Locate every Plasmodium parasite and every leukocyte.
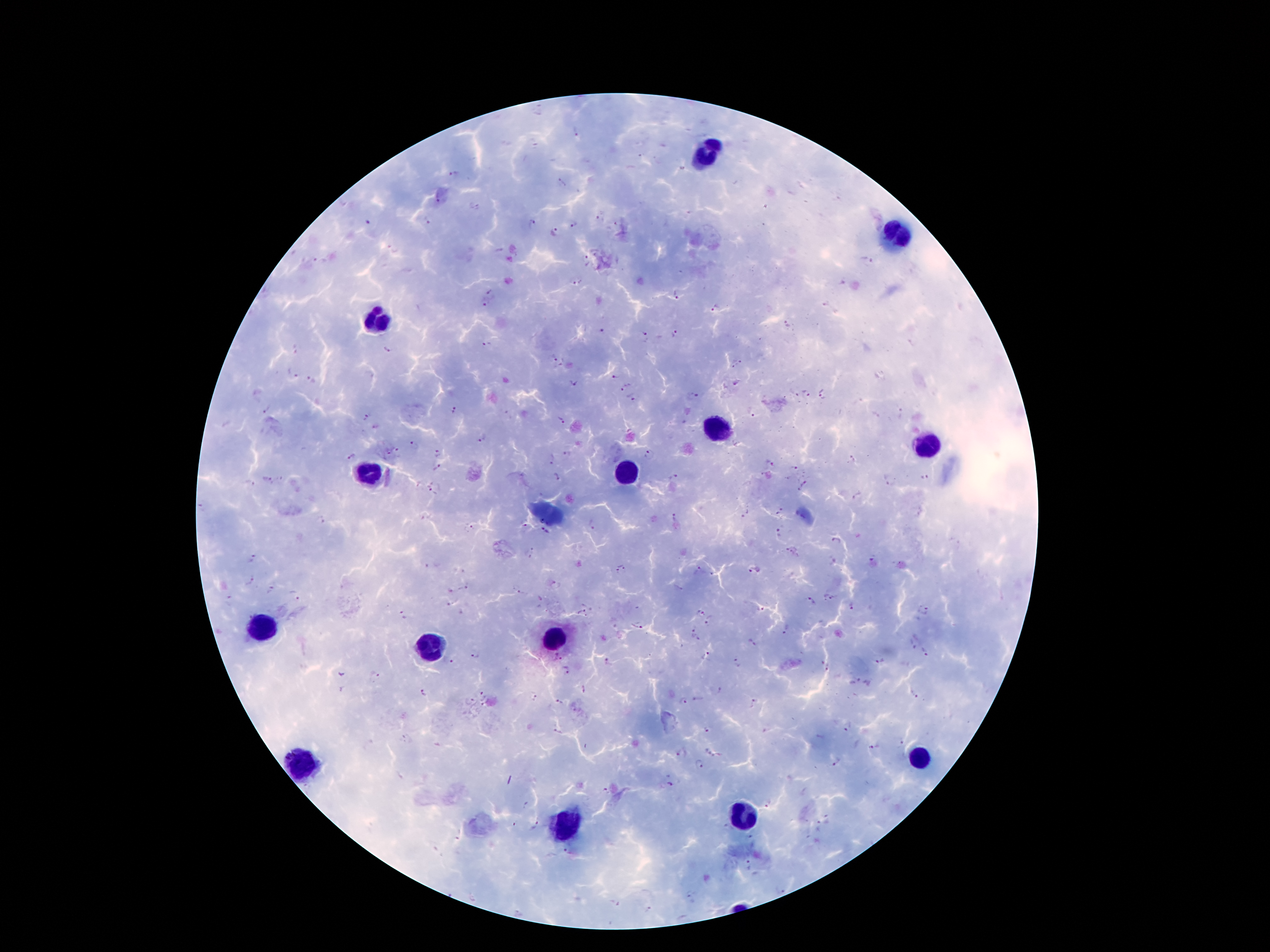

Approximate centers as (x, y) in pixels.
Plasmodium parasites: (538, 111), (577, 134), (452, 176), (560, 183), (437, 200), (473, 207), (427, 221), (531, 223), (572, 223), (553, 232), (391, 249), (586, 259), (316, 260), (867, 260), (577, 282), (492, 291), (676, 297), (486, 304), (716, 309), (788, 326), (601, 332), (676, 335), (647, 339), (487, 344), (297, 350), (386, 351), (552, 358), (736, 363), (291, 376), (613, 377), (312, 382), (573, 382), (625, 387), (806, 392), (792, 395), (823, 396), (631, 398), (692, 398), (267, 409), (456, 409), (748, 413), (901, 414), (874, 415), (366, 417), (559, 421), (483, 438), (414, 446), (399, 450), (386, 453), (440, 453), (566, 453), (650, 455), (350, 457), (851, 460), (552, 462), (768, 463), (438, 467), (795, 467), (925, 476), (557, 477), (673, 477), (886, 479), (268, 481), (247, 484), (804, 484), (433, 489), (858, 495), (781, 510), (744, 514), (426, 518), (673, 519), (321, 520), (539, 520), (590, 524), (525, 526), (469, 528), (544, 531), (778, 534), (836, 540), (790, 551), (531, 552), (251, 558), (870, 561), (430, 566), (622, 569), (698, 569), (754, 571), (250, 581), (555, 585), (466, 588), (270, 590), (520, 591), (295, 595), (827, 597), (230, 600), (810, 601), (447, 604), (851, 608), (761, 609), (923, 611), (700, 613), (581, 614), (403, 617), (709, 621), (637, 626), (786, 628), (692, 632), (752, 642), (912, 645), (926, 653), (474, 656), (706, 656), (556, 659), (449, 660), (880, 661), (607, 662), (738, 663), (824, 669), (342, 672), (567, 673), (376, 674), (585, 687), (343, 688), (721, 689), (423, 693), (483, 694), (914, 695), (535, 699), (697, 699), (468, 701), (559, 701), (684, 701), (754, 705), (847, 727), (557, 729), (707, 729), (406, 738), (901, 743), (873, 748), (711, 751), (681, 754), (838, 761), (699, 763), (669, 784), (607, 791), (525, 802), (766, 806), (535, 826), (750, 837), (566, 851), (748, 867), (616, 903), (649, 909).
Leukocytes: (710, 151), (896, 237), (378, 317), (717, 426), (923, 446), (370, 473), (626, 473), (261, 626), (555, 641), (429, 646), (921, 755), (303, 760), (740, 816), (569, 828).

Summary:
  - Image size: 1270×952 pixels
  - Capture: smartphone camera through the microscope eyepiece
  - Patient malaria status: positive for Plasmodium falciparum
  - Magnification: 100x
  - Preparation: thick blood film
  - Field of view: one from this slide
  - Stain: Giemsa